Name the parasite shown.
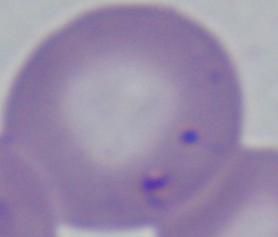
Babesia.

modality = photomicrograph
magnification = 1000x